Assess the morphology of the red blood cells.
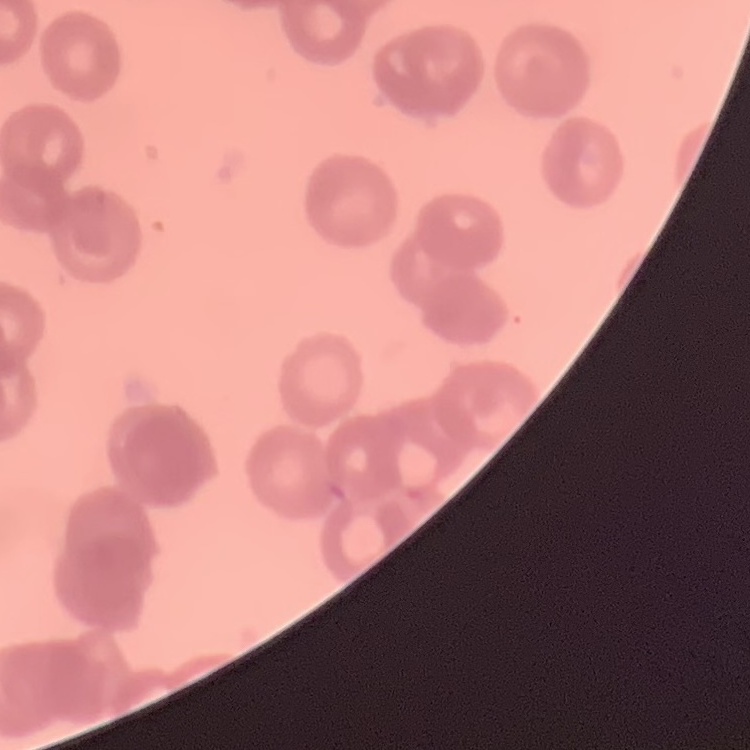

Rouleaux formation.

One tile cut from a larger photomicrograph. Field's or Giemsa stain. Thin blood smear.